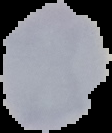 Image is 112×133 pixels. Result: no malaria parasites detected. From a thin blood film. Segmented cell region on a black background.